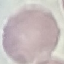
Summary:
  - Malaria status: uninfected
  - Image type: cell patch, automatically extracted from a larger field of view and resized to 64 × 64 pixels
  - Preparation: thin blood film
  - Capture: smartphone through the microscope eyepiece
  - Stain: Giemsa